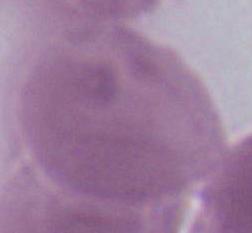
Micrograph. Captured at 1000x magnification. An erythrocyte is seen.